State the blood parasite species.
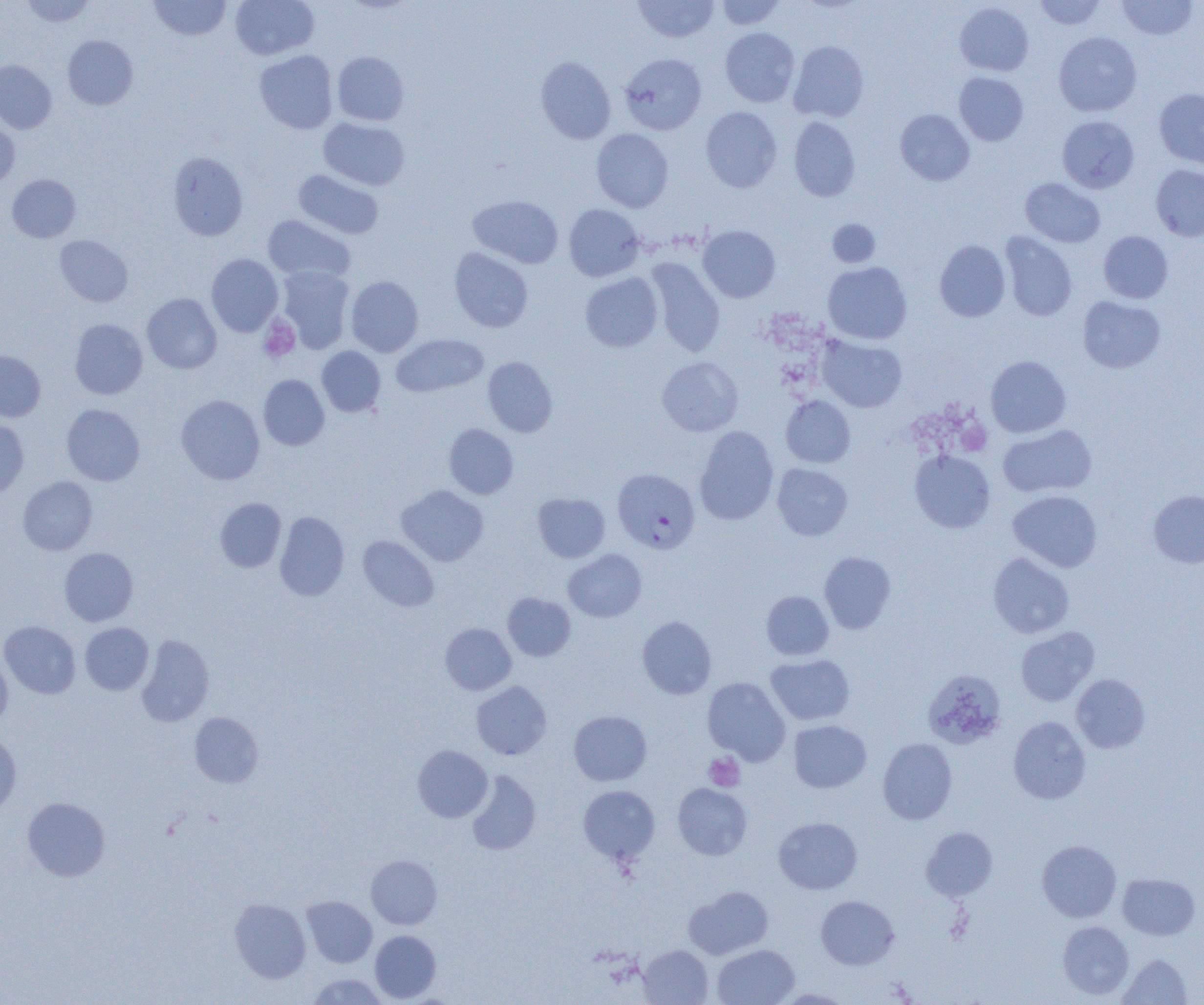
Plasmodium falciparum.

Approximate bounding boxes as [x1, y1, x2, y2] in pixels. Uninfected red blood cell locations: [21, 0, 96, 27], [230, 0, 319, 60], [716, 0, 787, 30], [1033, 0, 1106, 30], [1116, 0, 1199, 40], [148, 1, 232, 40], [633, 1, 719, 43], [955, 2, 1034, 76], [720, 28, 799, 107], [1054, 32, 1142, 117], [62, 35, 138, 110], [788, 41, 869, 122], [255, 50, 338, 134], [332, 51, 409, 126], [620, 53, 707, 135], [535, 56, 616, 144], [0, 59, 56, 134], [954, 72, 1028, 146], [1154, 88, 1204, 170], [701, 106, 782, 192], [895, 109, 974, 186], [1057, 116, 1139, 193], [789, 117, 860, 201], [318, 118, 409, 190], [0, 119, 19, 188], [591, 128, 673, 212], [168, 152, 248, 241], [1151, 164, 1204, 242], [294, 169, 384, 239], [7, 174, 80, 242], [1020, 178, 1105, 248], [468, 195, 563, 268], [564, 204, 645, 281], [263, 215, 355, 284], [827, 219, 881, 268], [698, 225, 781, 302], [1098, 230, 1173, 303], [1000, 232, 1077, 321], [54, 235, 133, 306], [934, 240, 1011, 322], [449, 248, 533, 332], [206, 254, 283, 336], [646, 258, 726, 357], [823, 261, 912, 344], [276, 267, 355, 354], [580, 272, 662, 352], [345, 275, 424, 357], [142, 293, 222, 374], [1078, 296, 1166, 373], [69, 318, 148, 399], [391, 334, 488, 397], [817, 335, 907, 412], [316, 346, 385, 417], [0, 350, 45, 421], [985, 355, 1071, 438], [483, 357, 557, 437], [657, 357, 743, 436], [258, 374, 329, 450], [176, 394, 265, 485], [781, 396, 855, 468], [62, 404, 145, 485], [0, 418, 29, 498], [444, 424, 518, 499], [998, 424, 1097, 498], [694, 426, 779, 525], [910, 450, 995, 533], [772, 463, 853, 540], [18, 476, 97, 555], [396, 485, 489, 566], [1008, 490, 1102, 572], [1149, 490, 1204, 568], [533, 493, 610, 562], [214, 498, 286, 572], [274, 511, 349, 601], [358, 535, 439, 611], [59, 547, 138, 626], [563, 549, 646, 622], [819, 552, 896, 633], [988, 552, 1074, 638], [761, 591, 833, 660], [502, 593, 576, 661], [637, 616, 716, 699], [0, 621, 81, 699], [80, 622, 154, 695], [440, 623, 516, 695], [1015, 627, 1099, 706], [136, 634, 214, 727], [0, 648, 12, 729], [766, 654, 855, 725], [922, 669, 1007, 749], [1071, 674, 1150, 753], [702, 677, 790, 765], [471, 681, 552, 759], [568, 710, 652, 786], [189, 712, 263, 787], [1008, 716, 1091, 804], [789, 720, 871, 793], [0, 732, 22, 818], [877, 738, 957, 824], [413, 745, 492, 822], [466, 770, 541, 855], [672, 783, 752, 860], [578, 785, 660, 865], [22, 796, 110, 881], [773, 817, 862, 894], [921, 826, 998, 901], [1037, 840, 1121, 922], [365, 855, 442, 928], [1117, 873, 1200, 940], [684, 886, 773, 959], [302, 896, 377, 968], [816, 896, 899, 969], [229, 899, 311, 983], [1057, 920, 1134, 1000], [370, 930, 441, 1002], [713, 944, 798, 1005], [638, 945, 713, 1004], [1117, 955, 1192, 1004], [306, 973, 390, 1004], [772, 989, 852, 1004]. Plasmodium falciparum-infected red blood cell locations: [610, 469, 698, 555]. Platelet locations: [258, 315, 300, 363], [703, 753, 744, 791]. Optical microscopy. Thin blood film. Single field of view. Image is 1204×1005 pixels. Captured at 1000x magnification.